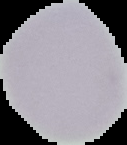
From a thin blood smear. Segmented cell region on a black background. Image is 127×145 pixels. Malaria status: uninfected.